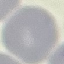
Result: no malaria parasites detected. Cell patch, automatically extracted from a larger field of view and resized to 64 × 64 pixels. Giemsa stain. Thin blood smear. Photographed with a smartphone camera at the microscope eyepiece.